State which cell type is depicted.
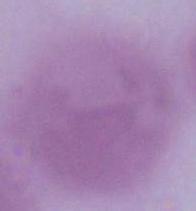
An erythrocyte.

Micrograph. 1000x magnification.